Assess this cell for malaria.
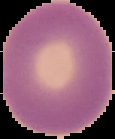
It is uninfected.

image_type: segmented cell region with the area outside set to black
image_size: 115×139 pixels
preparation: thin blood film